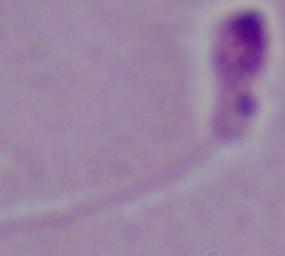 Micrograph. Captured at 1000x magnification. A Leishmania parasite is shown.